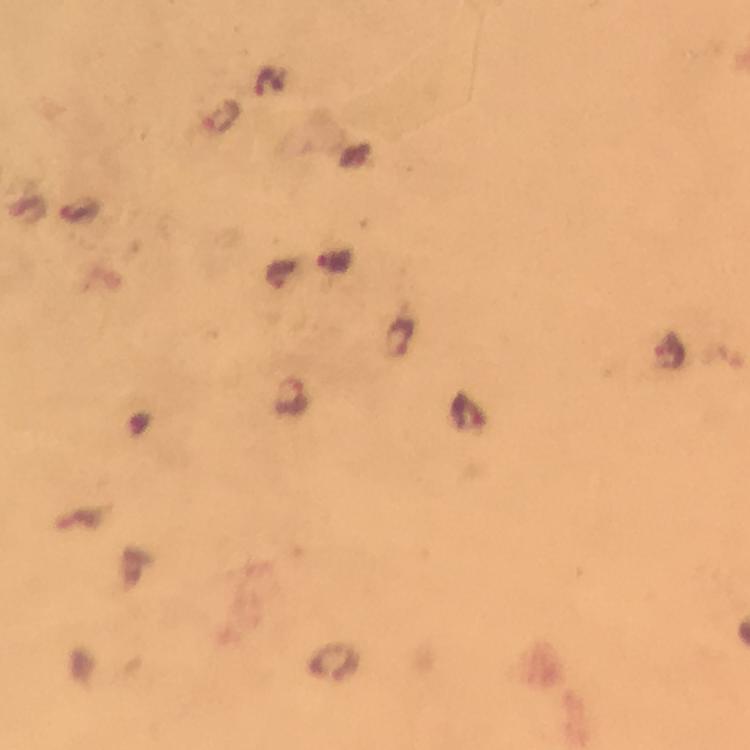 Approximate centers as (x, y) in pixels. Plasmodium parasite locations: (401, 338), (670, 356), (292, 397). Thick blood film. Giemsa-stained preparation. A crop from one field of view. At 100x magnification. Image is 750×750 pixels. From a diagnostic examination for malaria. Photographed through the microscope with a smartphone camera. Immersion oil was used.